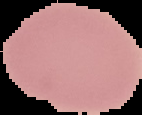

Segmented cell region on a black background. Image is 142×115 pixels. From a thin blood film. Result: negative for Plasmodium parasites.